Locate and identify every blood parasite.
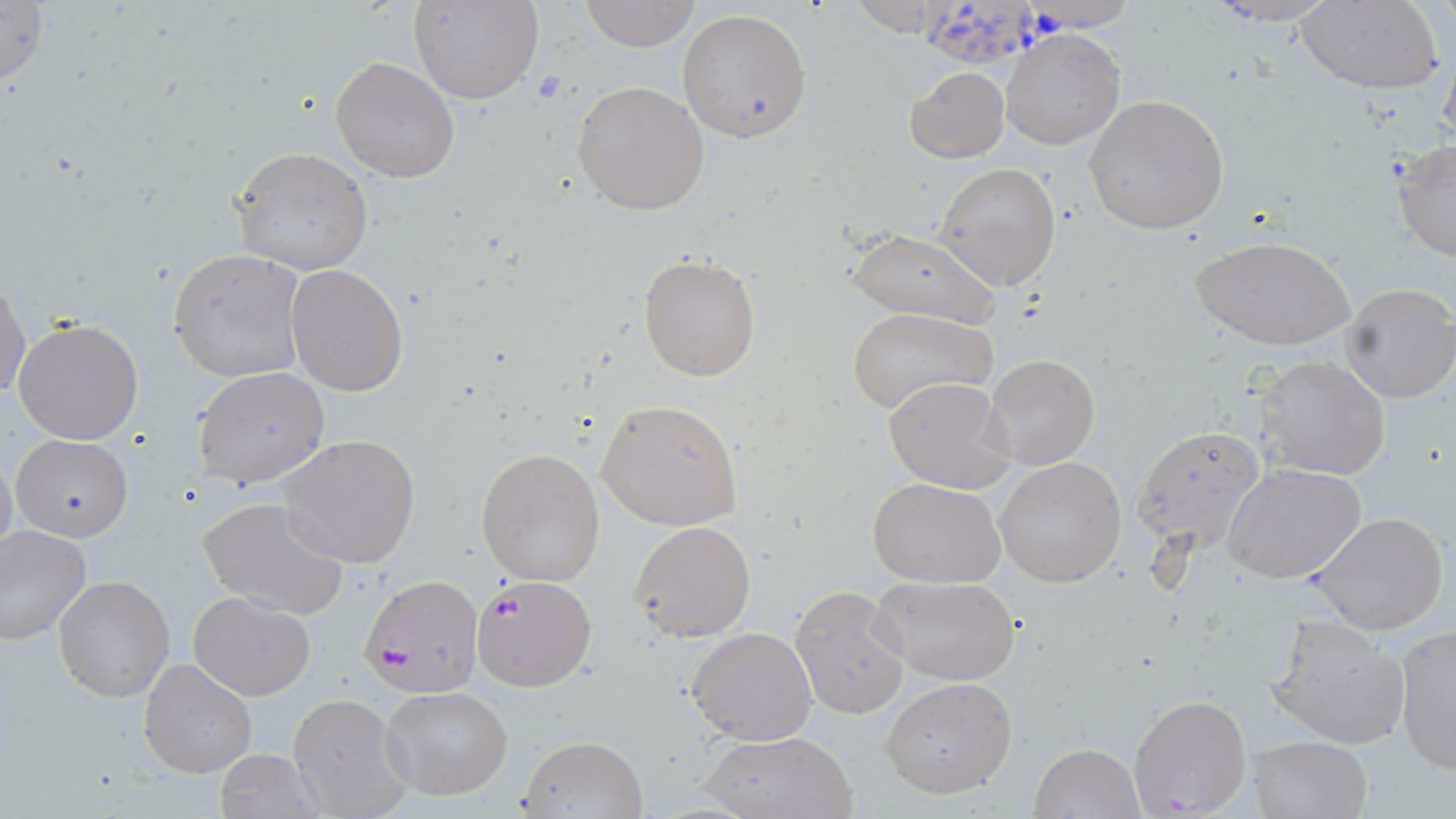
Approximate bounding boxes as (x1,y1)-(x2,y2) corner pairs in pixels.
Plasmodium falciparum-infected red blood cells: (360,574)-(483,697), (471,575)-(595,691).
No Plasmodium ovale, Plasmodium malariae, Plasmodium vivax, Babesia divergens, or Trypanosoma brucei observed.

{
  "slide_level_diagnosis": "Plasmodium falciparum",
  "modality": "light microscopy",
  "stain": "May-Grünwald-Giemsa",
  "uninfected_red_blood_cell_locations": "approximate bounding boxes as (x1,y1)-(x2,y2) corner pairs in pixels: (0,0)-(50,91), (412,0)-(543,104), (578,0)-(701,51), (1199,0)-(1341,27), (1295,1)-(1443,93), (920,6)-(1047,73), (677,8)-(814,144), (1002,30)-(1123,150), (330,56)-(459,184), (905,67)-(1008,163), (915,68)-(1026,247), (572,79)-(712,215), (1084,94)-(1229,235), (1392,140)-(1456,262), (229,146)-(374,276), (936,163)-(1061,289), (851,230)-(999,324), (1190,234)-(1355,350), (169,249)-(306,382), (638,253)-(761,380), (286,264)-(410,396), (0,274)-(29,403), (1339,280)-(1456,403), (845,307)-(995,417), (13,318)-(144,445), (986,354)-(1099,470), (1254,355)-(1390,480), (191,366)-(330,489), (884,376)-(1014,493), (597,400)-(743,530), (1133,425)-(1265,552), (12,434)-(133,541), (277,435)-(419,567), (475,447)-(605,585), (0,448)-(17,567), (994,457)-(1126,588), (1225,464)-(1368,584), (867,477)-(1008,586), (196,496)-(349,619), (1309,511)-(1449,636), (628,520)-(755,642), (0,524)-(92,646), (53,574)-(176,703), (868,574)-(1022,684), (791,586)-(911,719), (188,591)-(316,700), (1265,614)-(1410,751), (1392,624)-(1456,774), (687,627)-(817,745), (139,658)-(257,779), (881,676)-(1018,799), (381,685)-(512,801), (288,692)-(414,818), (1126,693)-(1251,817), (700,730)-(856,818), (517,733)-(649,819), (1246,735)-(1373,819), (1031,742)-(1144,818), (215,749)-(320,819)",
  "image_size": "1456×819 pixels",
  "field_of_view": "one of a larger specimen",
  "preparation": "thin blood film",
  "magnification": "1000x"
}